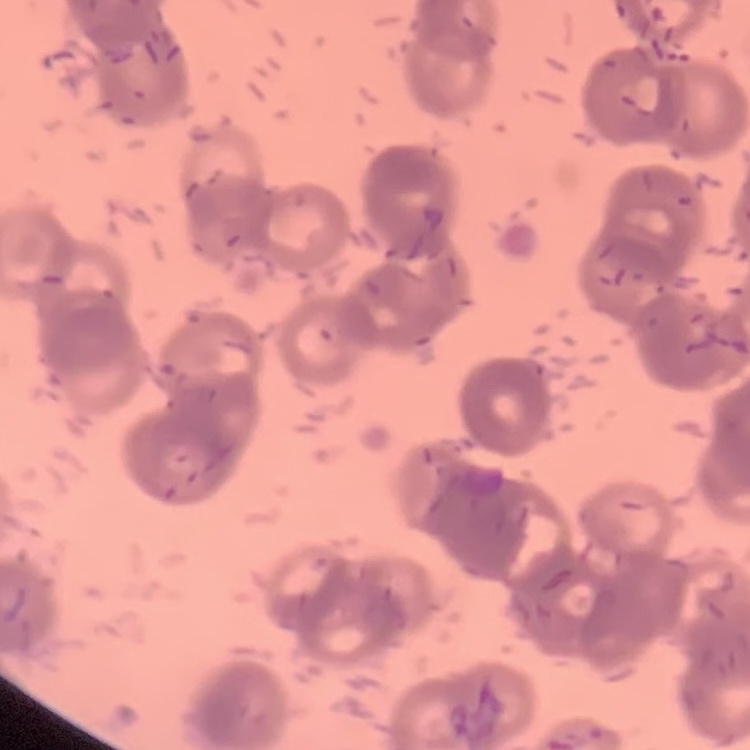
The red blood cells show rouleaux formation. Square crop of a larger photomicrograph. Thin peripheral smear. Stained with either Field's or Giemsa.